Comment on the morphology of the erythrocytes.
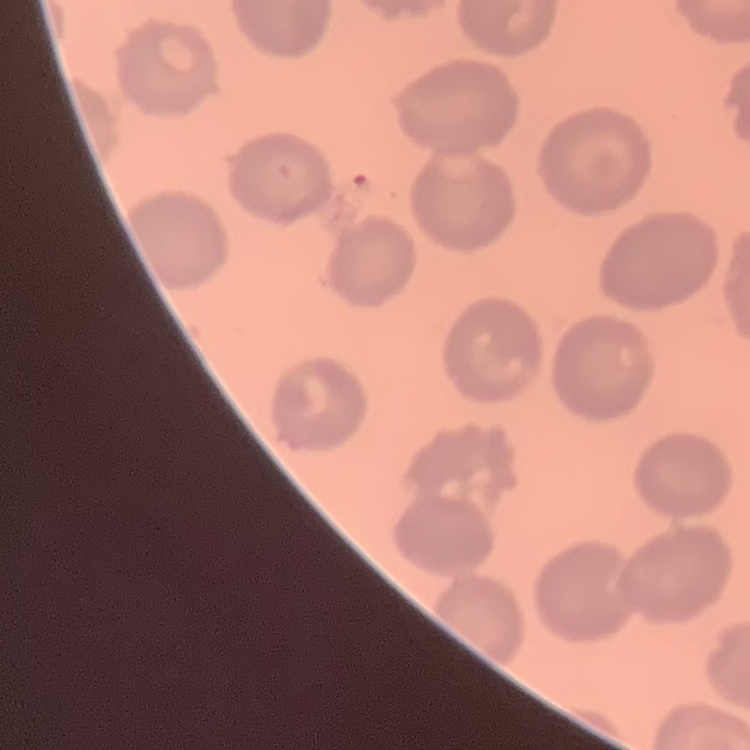
They show no rouleaux formation.

{
  "preparation": "thin peripheral smear",
  "image_type": "one tile cut from a larger photomicrograph",
  "stain": "Field's or Giemsa"
}